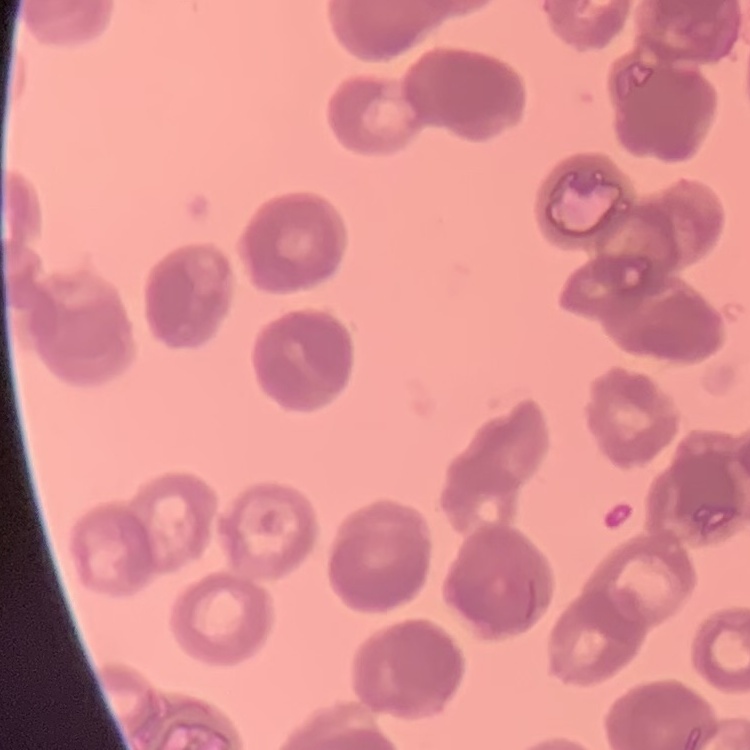

Summary:
  - Red blood cell morphology: rouleaux formation
  - Stain: Field's or Giemsa
  - Preparation: thin peripheral smear
  - Image type: one tile cut from a larger photomicrograph